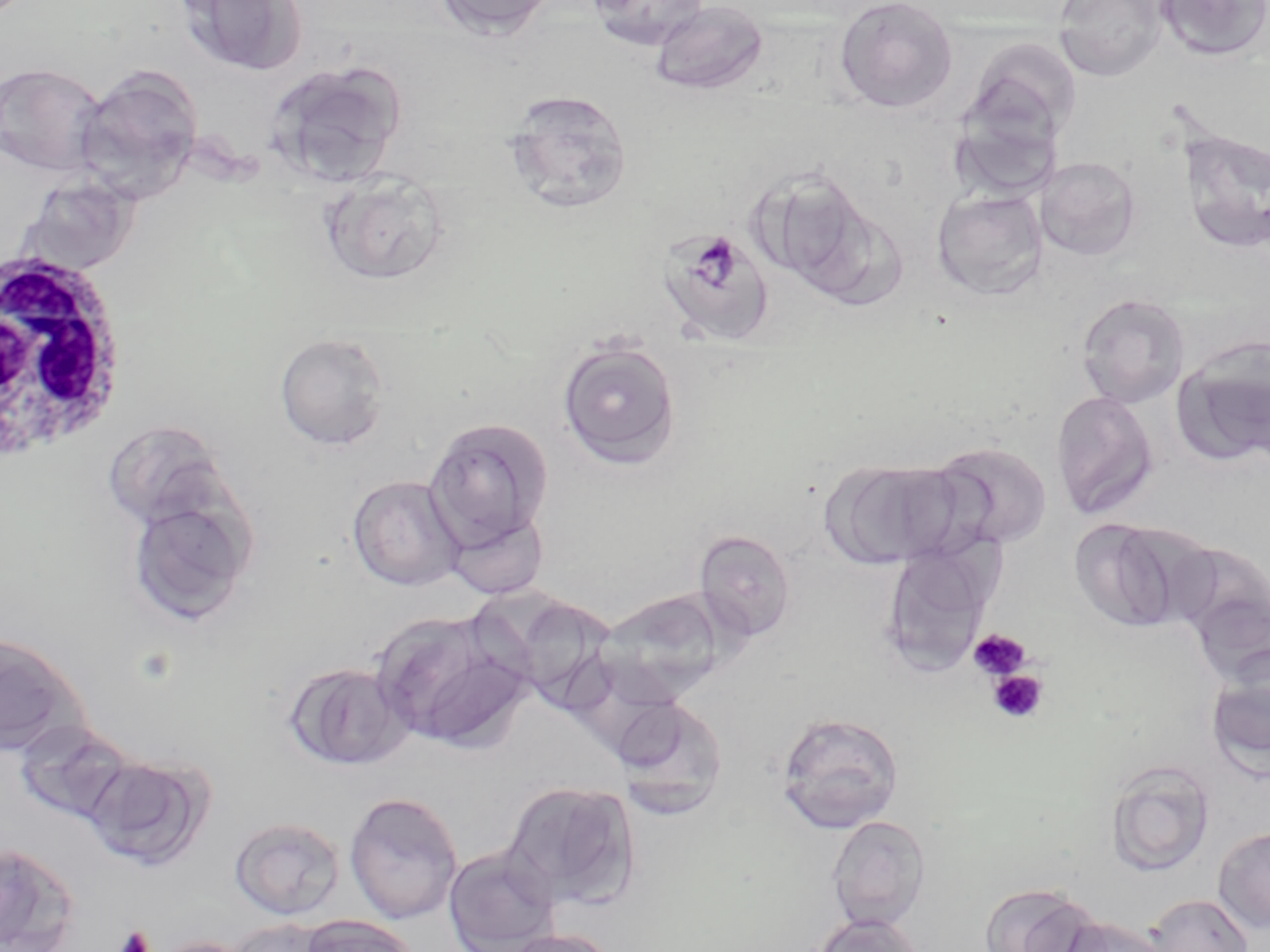
Approximate bounding boxes as named x1/y1/x2/y2 corners in pixels. Plasmodium malariae-infected red blood cell locations: (x1=655, y1=226, x2=777, y2=347). White blood cell locations: (x1=0, y1=245, x2=128, y2=463). Uninfected red blood cell locations: (x1=433, y1=0, x2=560, y2=40), (x1=584, y1=0, x2=710, y2=52), (x1=832, y1=0, x2=959, y2=113), (x1=1052, y1=0, x2=1169, y2=82), (x1=1154, y1=0, x2=1270, y2=62), (x1=177, y1=1, x2=306, y2=77), (x1=649, y1=1, x2=769, y2=96), (x1=962, y1=37, x2=1082, y2=149), (x1=265, y1=60, x2=406, y2=188), (x1=0, y1=62, x2=108, y2=178), (x1=73, y1=65, x2=205, y2=204), (x1=502, y1=89, x2=634, y2=216), (x1=1177, y1=128, x2=1270, y2=256), (x1=1035, y1=156, x2=1142, y2=261), (x1=755, y1=170, x2=891, y2=299), (x1=319, y1=171, x2=452, y2=288), (x1=14, y1=173, x2=142, y2=276), (x1=932, y1=188, x2=1048, y2=302), (x1=1074, y1=292, x2=1191, y2=409), (x1=273, y1=332, x2=393, y2=451), (x1=556, y1=338, x2=682, y2=470), (x1=1172, y1=340, x2=1270, y2=468), (x1=1051, y1=390, x2=1159, y2=521), (x1=424, y1=416, x2=553, y2=550), (x1=113, y1=433, x2=231, y2=530), (x1=930, y1=441, x2=1052, y2=550), (x1=824, y1=458, x2=969, y2=569), (x1=347, y1=475, x2=465, y2=591), (x1=126, y1=493, x2=255, y2=626), (x1=443, y1=507, x2=550, y2=600), (x1=1068, y1=517, x2=1198, y2=634), (x1=693, y1=529, x2=796, y2=643), (x1=1168, y1=540, x2=1270, y2=660), (x1=879, y1=543, x2=997, y2=676), (x1=477, y1=582, x2=593, y2=688), (x1=598, y1=589, x2=729, y2=703), (x1=369, y1=609, x2=530, y2=752), (x1=0, y1=631, x2=89, y2=759), (x1=1206, y1=650, x2=1270, y2=777), (x1=283, y1=661, x2=413, y2=771), (x1=611, y1=695, x2=729, y2=816), (x1=775, y1=710, x2=905, y2=833), (x1=13, y1=719, x2=136, y2=824), (x1=83, y1=752, x2=214, y2=872), (x1=1104, y1=760, x2=1216, y2=877), (x1=501, y1=779, x2=639, y2=910), (x1=344, y1=790, x2=463, y2=925), (x1=826, y1=815, x2=931, y2=931), (x1=229, y1=817, x2=345, y2=920), (x1=1213, y1=825, x2=1270, y2=934), (x1=0, y1=840, x2=79, y2=952), (x1=442, y1=846, x2=560, y2=951), (x1=977, y1=881, x2=1108, y2=952), (x1=1146, y1=893, x2=1253, y2=952), (x1=809, y1=912, x2=924, y2=952), (x1=297, y1=914, x2=422, y2=952), (x1=1061, y1=917, x2=1170, y2=952), (x1=225, y1=918, x2=335, y2=952), (x1=499, y1=929, x2=619, y2=952), (x1=149, y1=936, x2=256, y2=952). Platelet locations: (x1=968, y1=627, x2=1032, y2=680), (x1=987, y1=669, x2=1049, y2=724), (x1=113, y1=926, x2=154, y2=952). Slide-level diagnosis: Plasmodium malariae. 1000x magnification. May-Grünwald-Giemsa stain. One field of a larger specimen. Optical microscopy. Image is 1270×952 pixels. Thin blood smear.